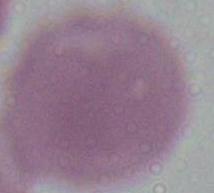
Summary:
  - Identification: red blood cell
  - Modality: photomicrograph
  - Magnification: 1000x